Name the parasite shown.
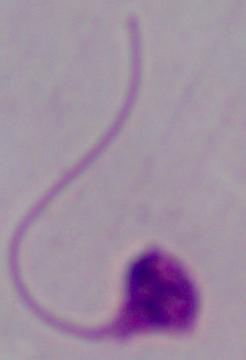
This is Leishmania.

{
  "modality": "photomicrograph",
  "magnification": "1000x"
}